Locate every leukocyte (white blood cell).
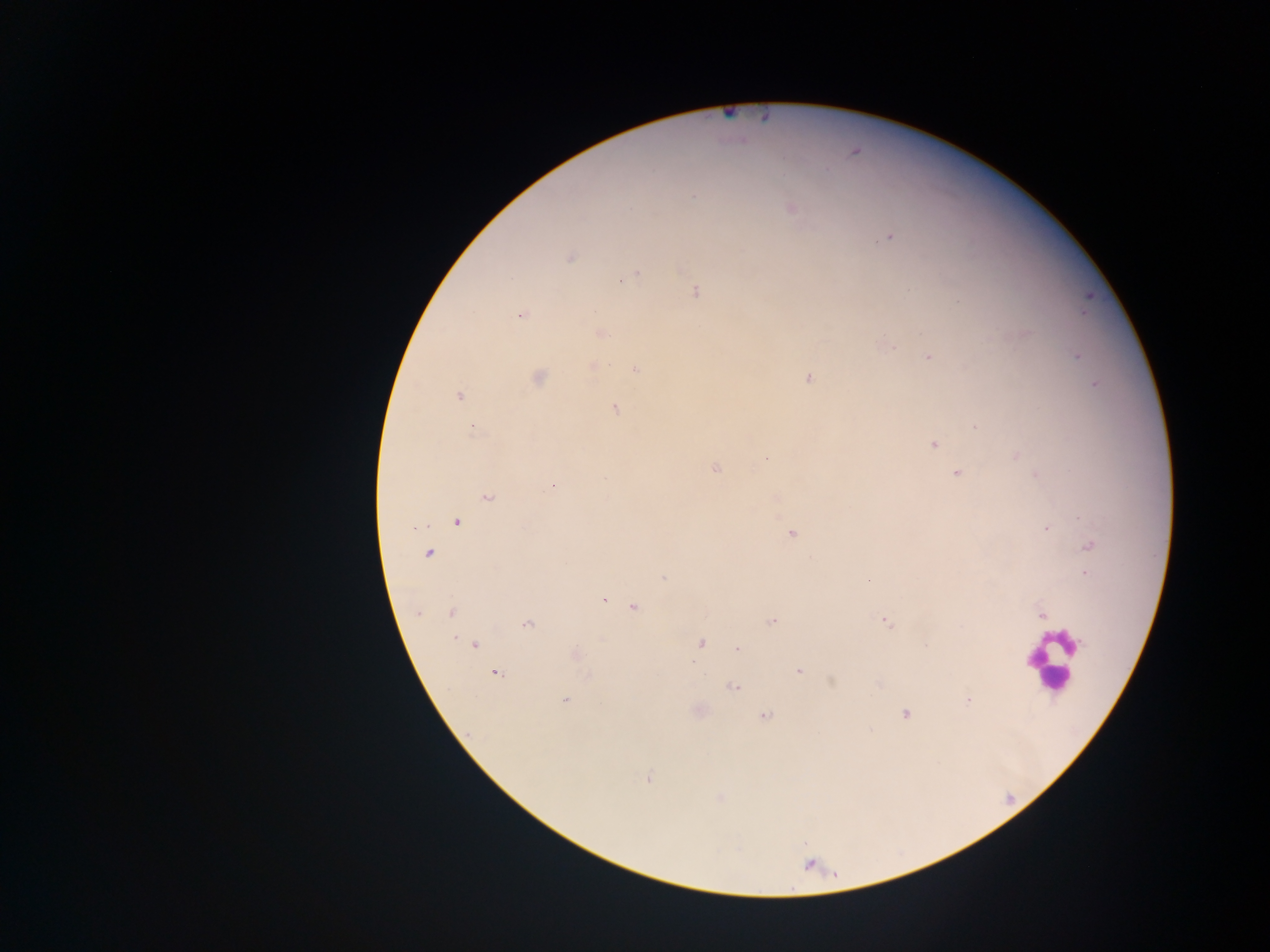
Approximate centers as (x, y) in pixels.
Leukocytes: (1051, 660).

Malaria parasite locations: (694, 196), (790, 208), (890, 238), (570, 257), (636, 274), (695, 292), (521, 315), (603, 333), (892, 347), (1077, 356), (928, 357), (592, 366), (634, 370), (808, 377), (537, 378), (1095, 385), (458, 396), (615, 409), (976, 427), (473, 428), (934, 445), (1016, 456), (765, 459), (715, 469), (957, 474), (1035, 475), (605, 477), (553, 485), (489, 497), (457, 522), (414, 528), (1046, 529), (792, 534), (1089, 546), (428, 554), (1084, 573), (664, 578), (868, 580), (604, 600), (634, 607), (451, 612), (418, 613), (1041, 615), (772, 620), (886, 622), (527, 624), (701, 643), (474, 645), (737, 649), (577, 655), (693, 661), (798, 670), (496, 673), (587, 676), (733, 687), (566, 700), (968, 700), (905, 714), (765, 716), (648, 778). Photographed through a microscope with a mobile-phone camera. Collected in Ghana. One field of view. Image is 1270×952 pixels. Thick blood film.